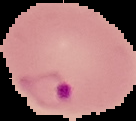

Summary:
  - Image type: segmented cell region on a black background
  - Result: Plasmodium parasites identified
  - Image size: 136×121 pixels
  - Preparation: thin blood smear